Identify the parasite.
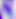

Toxoplasma gondii.

modality = micrograph
magnification = 400x